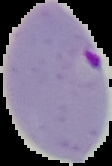
Cell region segmented out of the field of view; the surrounding area is masked to black. From a thin blood film. Malaria status: parasitized. Image is 112×166 pixels.